Locate every blood parasite and identify its species.
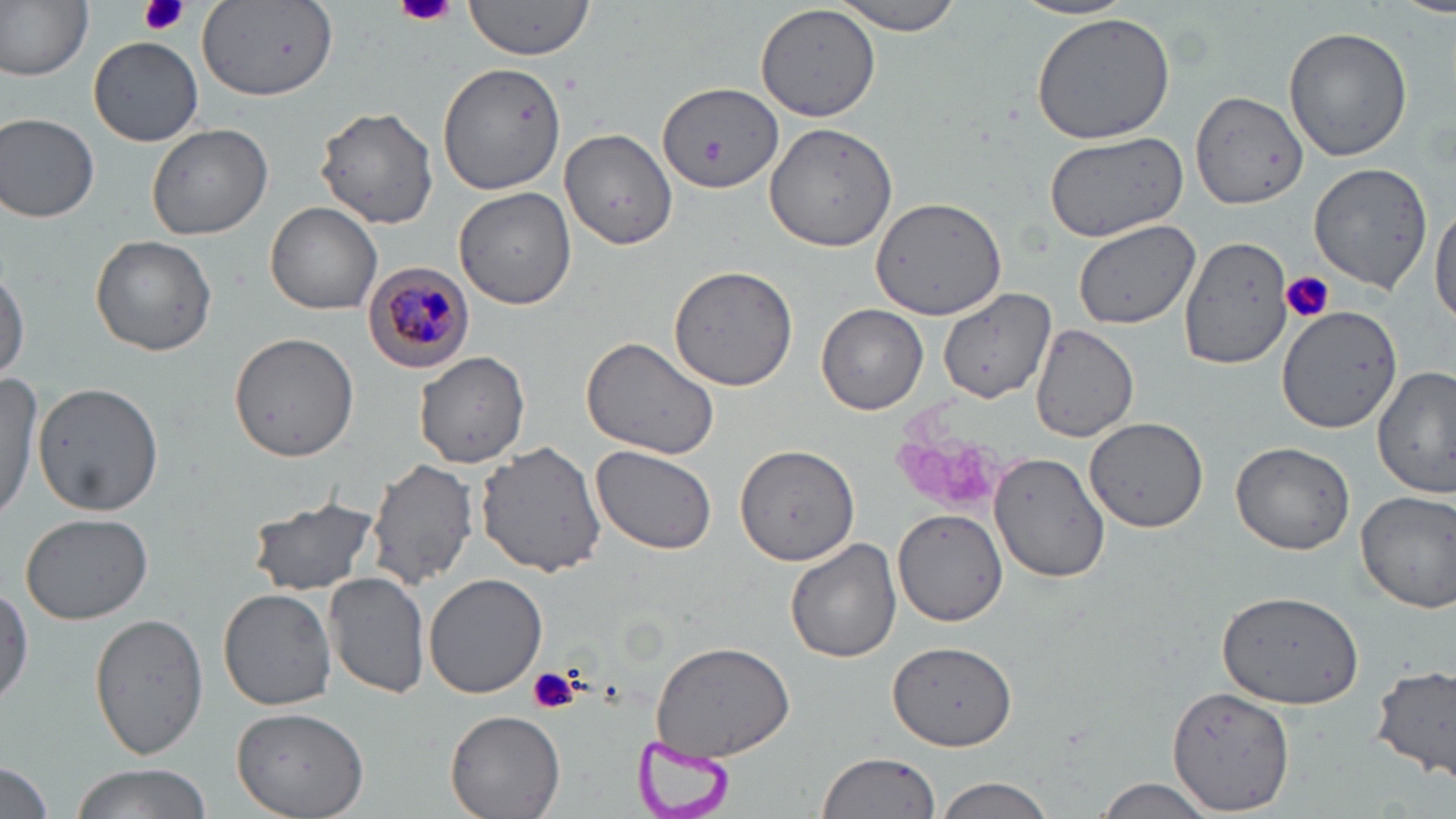
Approximate bounding boxes as (x1, y1, x2, y2) in pixels.
Plasmodium malariae-infected red blood cells: (364, 264, 475, 371).
No Plasmodium falciparum, Plasmodium ovale, Plasmodium vivax, Babesia divergens, or Trypanosoma brucei observed.

Platelet locations: (139, 0, 190, 37), (394, 0, 460, 27), (1280, 272, 1334, 322), (527, 664, 580, 714). Uninfected red blood cell locations: (0, 0, 92, 80), (465, 0, 595, 61), (828, 0, 964, 34), (1015, 0, 1139, 21), (1385, 0, 1456, 15), (198, 2, 336, 101), (756, 3, 881, 122), (1028, 9, 1178, 145), (1283, 25, 1412, 162), (88, 36, 205, 148), (439, 63, 565, 194), (655, 81, 784, 195), (1190, 89, 1308, 210), (311, 104, 439, 230), (0, 111, 100, 224), (763, 121, 900, 250), (147, 123, 273, 240), (560, 129, 678, 250), (1040, 132, 1190, 240), (1309, 162, 1432, 295), (454, 188, 577, 311), (870, 195, 1011, 321), (1430, 199, 1456, 332), (264, 201, 382, 315), (1072, 220, 1199, 329), (1175, 233, 1296, 372), (90, 235, 217, 356), (0, 262, 28, 382), (668, 264, 801, 394), (936, 286, 1055, 404), (818, 304, 928, 417), (1276, 304, 1401, 433), (1030, 324, 1137, 443), (228, 333, 358, 464), (579, 336, 722, 460), (413, 352, 532, 467), (1374, 368, 1453, 498), (0, 374, 43, 528), (32, 381, 163, 515), (1086, 418, 1210, 534), (476, 440, 607, 578), (1231, 441, 1355, 556), (736, 443, 860, 565), (592, 446, 717, 556), (990, 452, 1109, 583), (367, 459, 479, 590), (1354, 488, 1456, 613), (246, 497, 379, 596), (893, 508, 1008, 626), (18, 511, 153, 624), (785, 539, 902, 664), (422, 571, 548, 699), (322, 573, 431, 700), (218, 587, 337, 712), (1215, 592, 1363, 708), (89, 612, 209, 762), (649, 639, 796, 763), (887, 641, 1018, 751), (1371, 664, 1456, 782), (1166, 684, 1295, 814), (232, 707, 369, 819), (444, 710, 565, 819), (815, 751, 943, 819), (0, 760, 56, 819), (66, 762, 212, 819), (933, 776, 1056, 818), (1091, 778, 1219, 818). Slide-level diagnosis: Plasmodium malariae. May-Grünwald-Giemsa stain. Single field of view. Thin blood smear. Image is 1456×819 pixels. 1000x magnification. Optical microscopy.